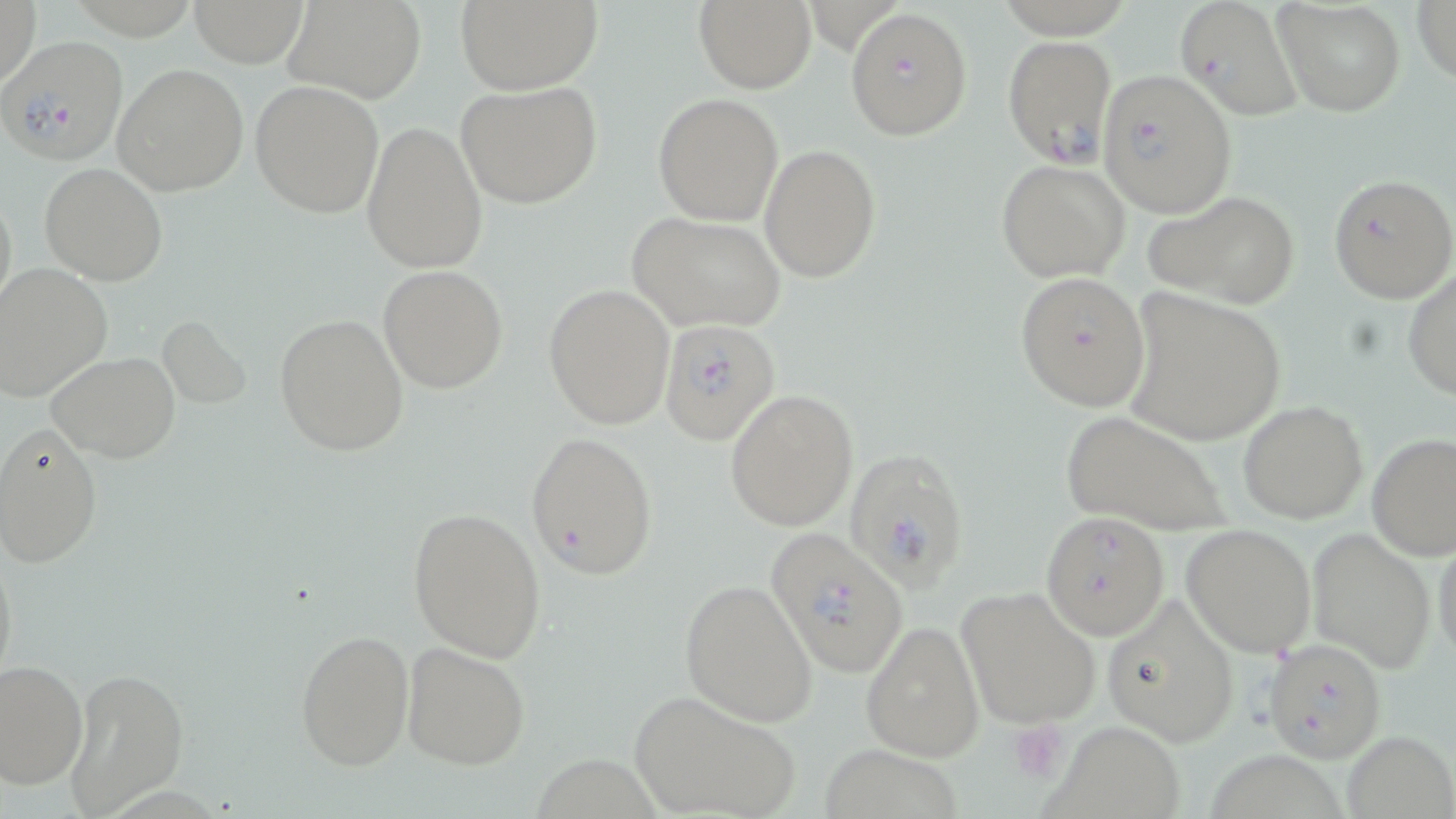
Summary:
  - Coordinate format: approximate bounding boxes as [x1, y1, x2, y2] in pixels
  - Plasmodium falciparum-infected red blood cell locations: [845, 7, 972, 142], [1002, 34, 1115, 167], [0, 36, 128, 165], [1095, 71, 1235, 220], [1329, 173, 1455, 303], [657, 320, 781, 445], [845, 447, 972, 588], [762, 527, 911, 676], [1262, 638, 1387, 762]
  - Uninfected red blood cell locations: [1, 0, 42, 95], [183, 0, 314, 66], [283, 0, 427, 104], [454, 0, 601, 92], [693, 0, 817, 93], [1174, 0, 1304, 122], [1272, 0, 1406, 117], [1412, 0, 1456, 87], [112, 62, 249, 197], [455, 79, 602, 211], [250, 80, 384, 218], [653, 93, 784, 226], [361, 121, 488, 272], [760, 144, 880, 282], [997, 160, 1130, 282], [39, 162, 168, 285], [0, 181, 17, 317], [1145, 189, 1302, 310], [626, 212, 787, 332], [0, 264, 112, 403], [378, 265, 509, 392], [1402, 268, 1456, 400], [1014, 270, 1151, 411], [544, 284, 675, 429], [1123, 288, 1285, 447], [274, 313, 410, 456], [157, 314, 251, 407], [47, 351, 182, 463], [724, 388, 859, 530], [1238, 399, 1369, 522], [1061, 410, 1230, 536], [0, 424, 103, 568], [526, 430, 659, 579], [1367, 432, 1456, 560], [409, 506, 548, 661], [1041, 511, 1169, 639], [1182, 521, 1316, 657], [1306, 527, 1438, 674], [1431, 533, 1455, 664], [0, 544, 17, 691], [681, 578, 819, 727], [957, 584, 1102, 727], [1100, 595, 1242, 747], [860, 618, 983, 761], [296, 627, 415, 770], [401, 640, 531, 770], [1, 660, 88, 789], [64, 668, 186, 816], [627, 690, 804, 819], [1048, 718, 1182, 813], [1341, 730, 1455, 819], [819, 743, 967, 818], [1199, 751, 1349, 819]
  - Platelet locations: [1011, 719, 1071, 783]
  - Slide-level diagnosis: Plasmodium falciparum
  - Stain: May-Grünwald-Giemsa
  - Modality: light microscopy
  - Image size: 1456×819 pixels
  - Magnification: 1000x
  - Field of view: one of a larger specimen
  - Preparation: thin blood smear